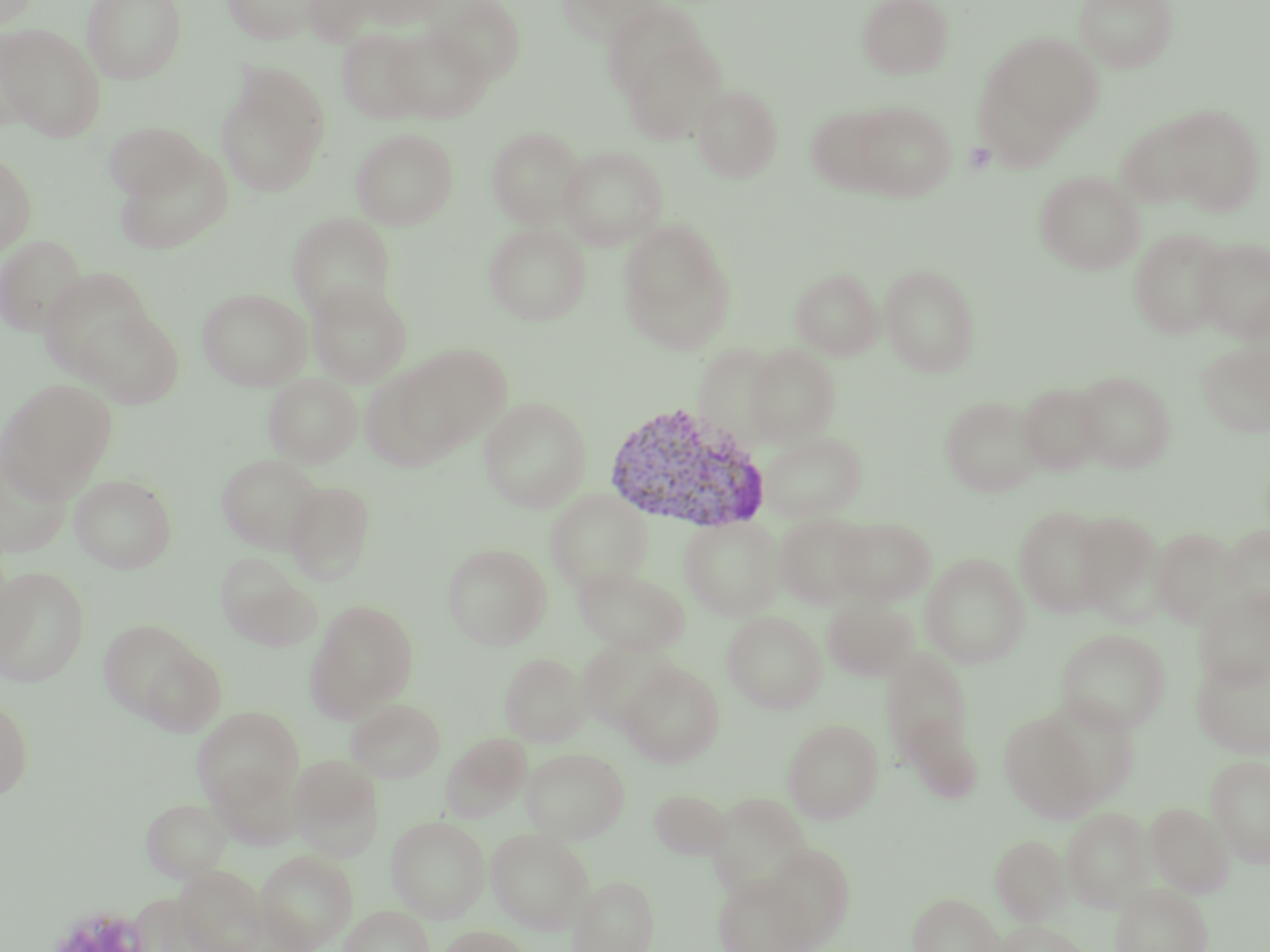
Approximate bounding boxes as (x1, y1, x2, y2) in pixels. Uninfected red blood cell locations: (0, 0, 41, 29), (81, 0, 187, 84), (221, 0, 323, 44), (301, 0, 385, 46), (352, 0, 447, 29), (426, 0, 526, 84), (558, 0, 665, 44), (857, 0, 954, 79), (1073, 0, 1178, 73), (601, 1, 711, 103), (0, 23, 106, 142), (384, 27, 492, 123), (337, 28, 429, 123), (984, 31, 1104, 142), (621, 37, 727, 145), (215, 66, 330, 198), (692, 84, 783, 182), (850, 100, 957, 201), (1161, 104, 1267, 215), (807, 105, 899, 196), (1116, 115, 1212, 209), (103, 121, 205, 201), (487, 126, 586, 228), (350, 128, 458, 229), (112, 146, 234, 255), (558, 146, 668, 250), (0, 151, 37, 256), (1035, 170, 1145, 274), (287, 213, 396, 320), (617, 220, 734, 350), (483, 223, 591, 326), (1129, 227, 1230, 339), (0, 235, 87, 336), (1193, 237, 1270, 341), (879, 263, 981, 377), (790, 267, 884, 360), (39, 268, 155, 380), (306, 279, 412, 387), (197, 287, 311, 390), (75, 306, 184, 408), (1197, 339, 1270, 438), (395, 343, 511, 453), (744, 343, 842, 446), (359, 365, 460, 472), (1074, 370, 1176, 472), (264, 374, 362, 467), (1, 379, 117, 499), (1017, 383, 1107, 475), (940, 395, 1042, 497), (479, 397, 591, 513), (761, 431, 867, 522), (0, 449, 72, 559), (216, 453, 325, 553), (70, 474, 177, 573), (284, 481, 375, 583), (545, 489, 653, 593), (1014, 505, 1112, 618), (1073, 511, 1161, 618), (774, 513, 875, 608), (678, 516, 786, 621), (831, 516, 937, 605), (1221, 524, 1270, 613), (1151, 527, 1238, 627), (442, 543, 551, 650), (216, 554, 316, 647), (921, 554, 1029, 668), (573, 565, 689, 656), (0, 566, 90, 686), (1195, 586, 1270, 689), (823, 596, 917, 680), (308, 601, 419, 719), (722, 611, 827, 713), (99, 619, 203, 722), (1056, 629, 1170, 734), (577, 642, 677, 733), (138, 644, 227, 736), (881, 647, 974, 764), (500, 652, 589, 746), (1192, 654, 1270, 759), (619, 661, 724, 766), (0, 695, 33, 801), (345, 698, 445, 782), (193, 706, 303, 810), (1000, 711, 1102, 823), (898, 713, 983, 802), (782, 718, 883, 823), (442, 733, 532, 821), (520, 747, 630, 843), (290, 754, 384, 860), (1206, 756, 1270, 868), (210, 762, 301, 850), (648, 789, 730, 859), (707, 793, 812, 898), (141, 798, 232, 882), (1145, 802, 1234, 898), (1061, 807, 1154, 913), (386, 816, 490, 922), (486, 828, 594, 933), (991, 834, 1072, 925), (763, 843, 855, 948), (255, 850, 357, 951), (713, 871, 821, 952), (569, 875, 658, 952), (1110, 883, 1212, 952), (908, 892, 1004, 952), (339, 905, 434, 952), (994, 919, 1091, 952), (439, 925, 530, 952). Plasmodium vivax-infected red blood cell locations: (601, 402, 770, 536). Platelet locations: (965, 141, 997, 174). Slide-level diagnosis: Plasmodium vivax. Thin blood film. Image is 1270×952 pixels. Captured at 1000x magnification. Single field of view. May-Grünwald-Giemsa stain. Light microscopy.